Locate every malaria parasite.
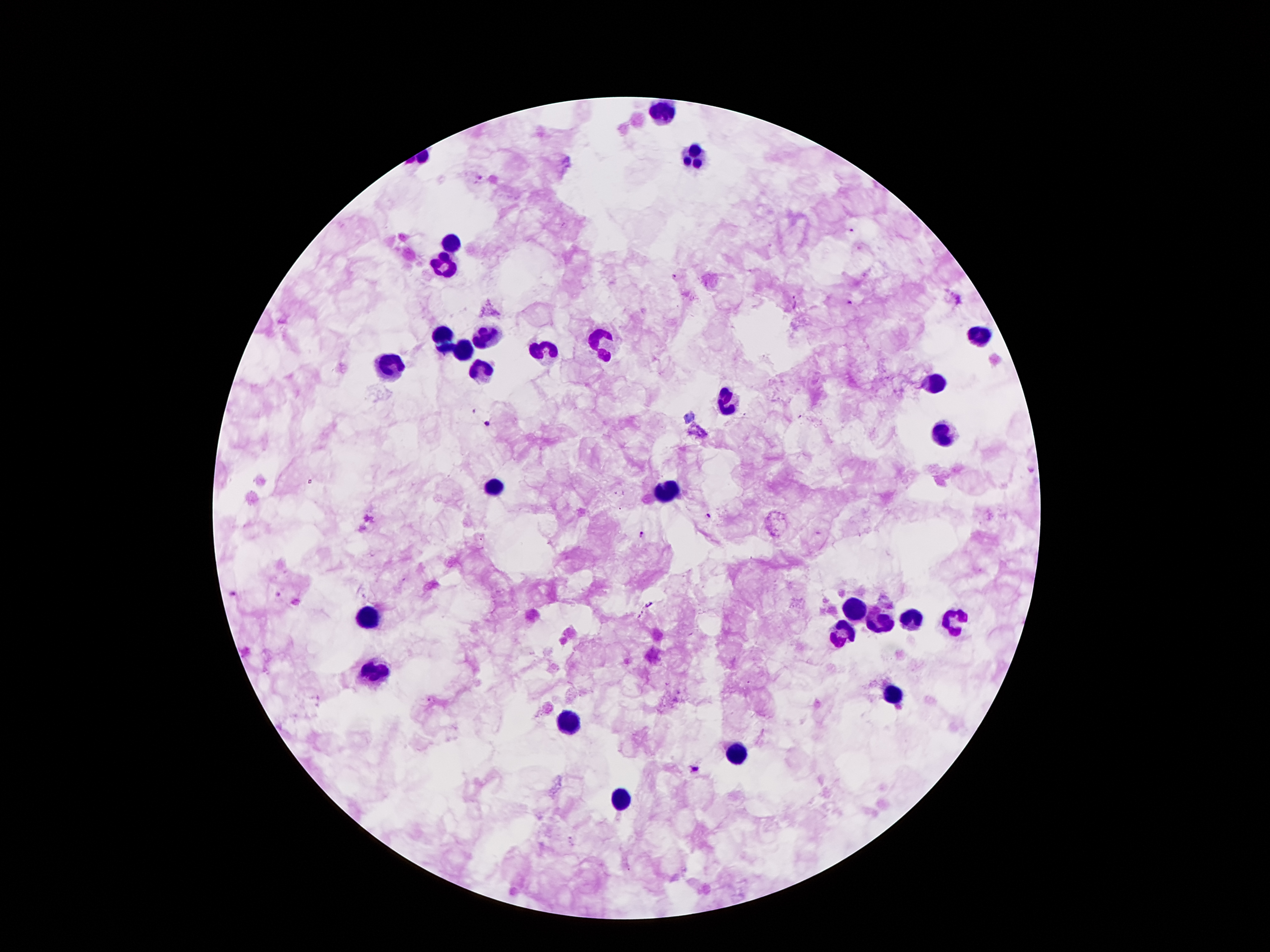

Approximate centers as {x, y} in pixels.
Malaria parasites: {481, 177}, {851, 231}, {956, 300}, {851, 302}, {485, 421}, {707, 516}, {640, 535}, {235, 594}, {648, 604}, {694, 770}.

{
  "field_of_view": "single",
  "preparation": "thick peripheral-blood smear",
  "leukocyte_locations": "approximate centers as {x, y} in pixels: {662, 113}, {694, 157}, {450, 241}, {446, 262}, {482, 333}, {444, 336}, {980, 336}, {599, 342}, {463, 351}, {543, 351}, {389, 365}, {480, 371}, {929, 381}, {726, 403}, {942, 430}, {497, 485}, {669, 489}, {856, 608}, {368, 616}, {910, 616}, {879, 619}, {955, 619}, {839, 633}, {375, 670}, {891, 695}, {566, 723}, {734, 755}, {625, 798}",
  "capture": "smartphone camera through the microscope eyepiece",
  "patient_malaria_status": "positive for Plasmodium falciparum",
  "magnification": "100x",
  "stain": "Giemsa",
  "image_size": "1270×952 pixels"
}